Give the preparation type.
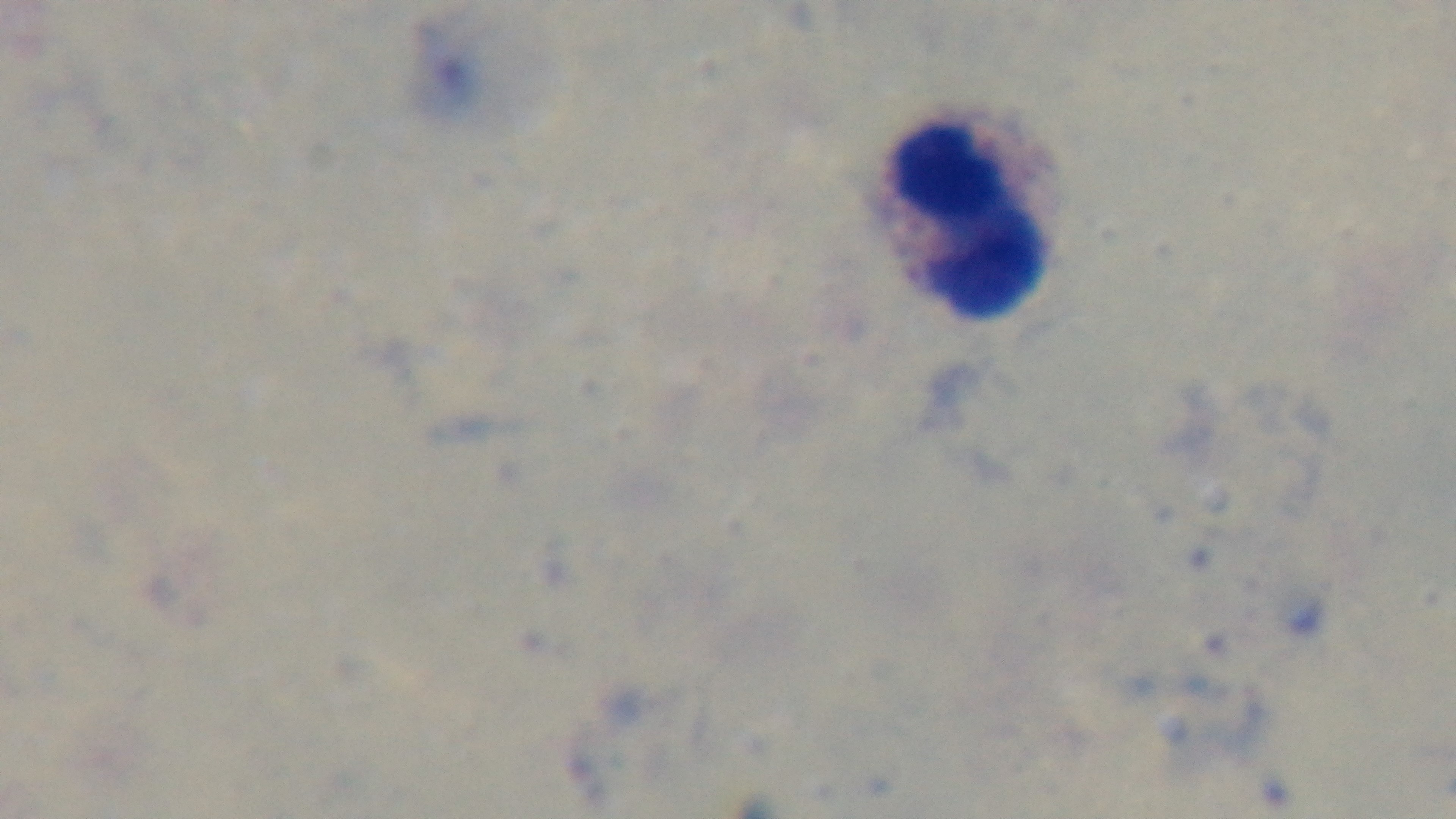

A thick smear.

Malaria status: uninfected. Photomicrograph. Mounted 4K digital camera. 100x oil-immersion objective. Giemsa-stained. Single field of view.